Evaluate for Plasmodium parasites.
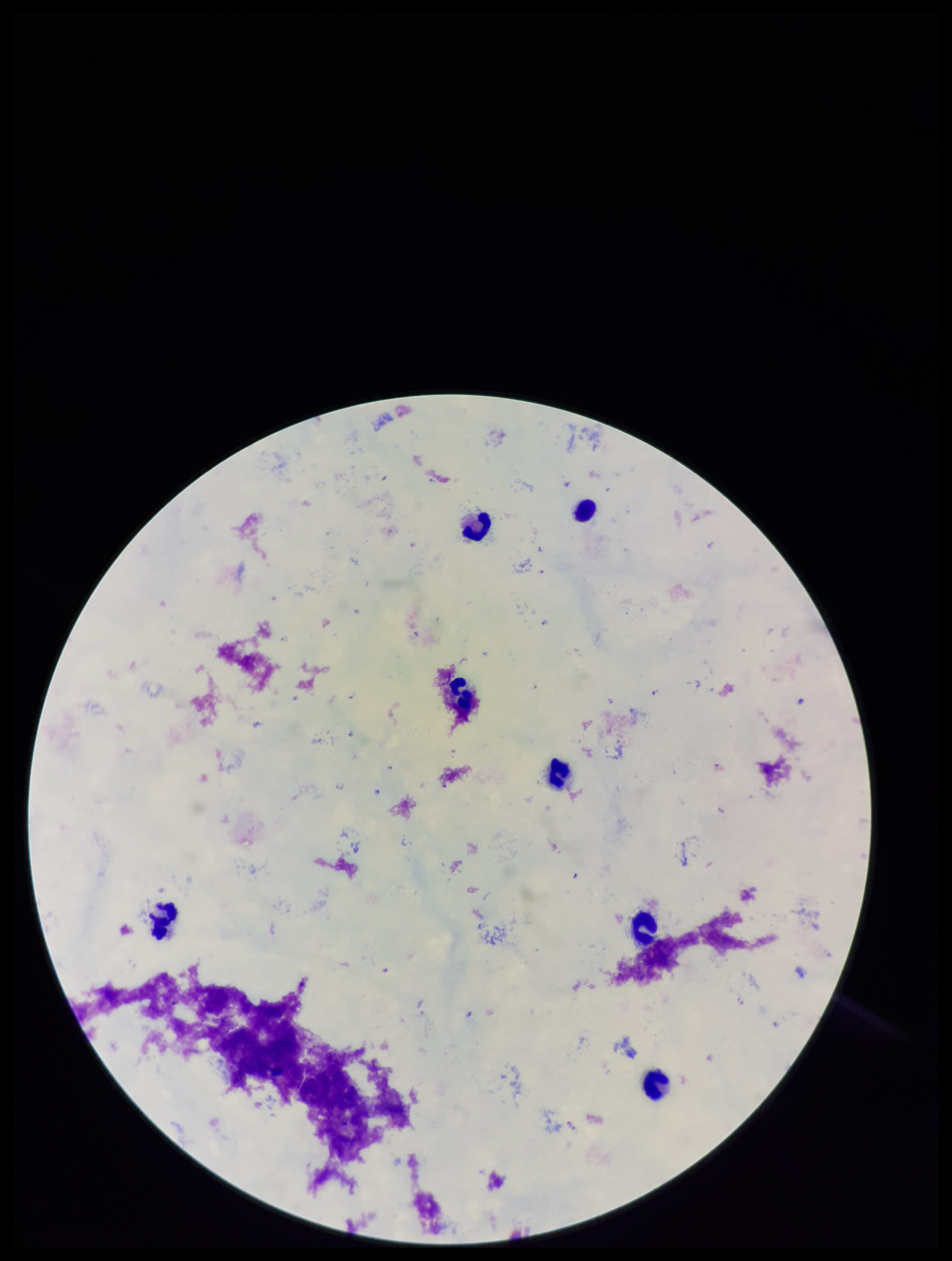
Seen.

Stained with Giemsa. Preparation: thick smear. Patient malaria status: positive. Leukocyte count: 7. Image is 952×1261 pixels. Parasite count: 14. One field from this slide. Species reported for this patient: Plasmodium falciparum. Photographed through the microscope eyepiece with a smartphone camera.